Comment on the morphology of the red blood cells.
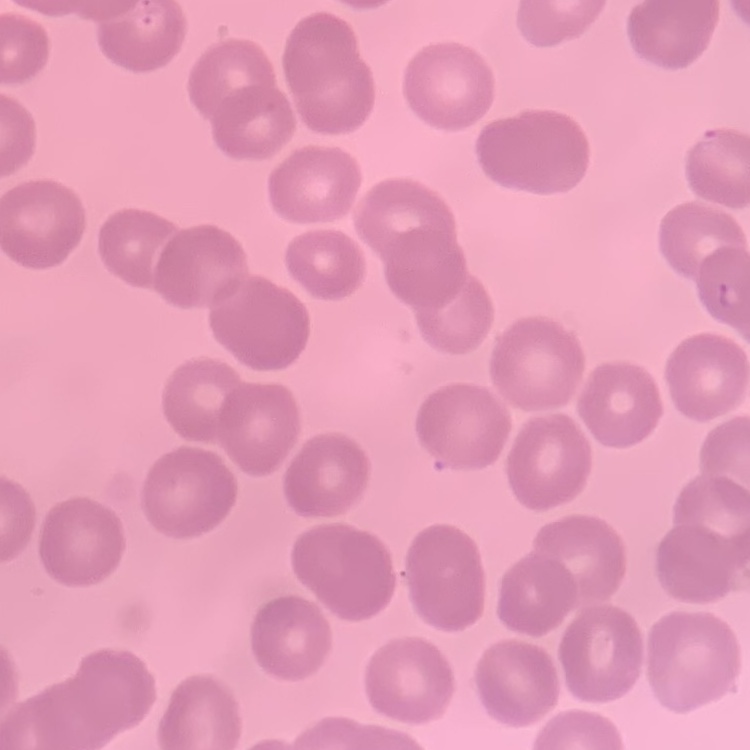

No rouleaux formation.

Summary:
  - Stain: Field's or Giemsa
  - Preparation: thin peripheral smear
  - Image type: one tile cut from a larger photomicrograph